Assess for parasitized red blood cells.
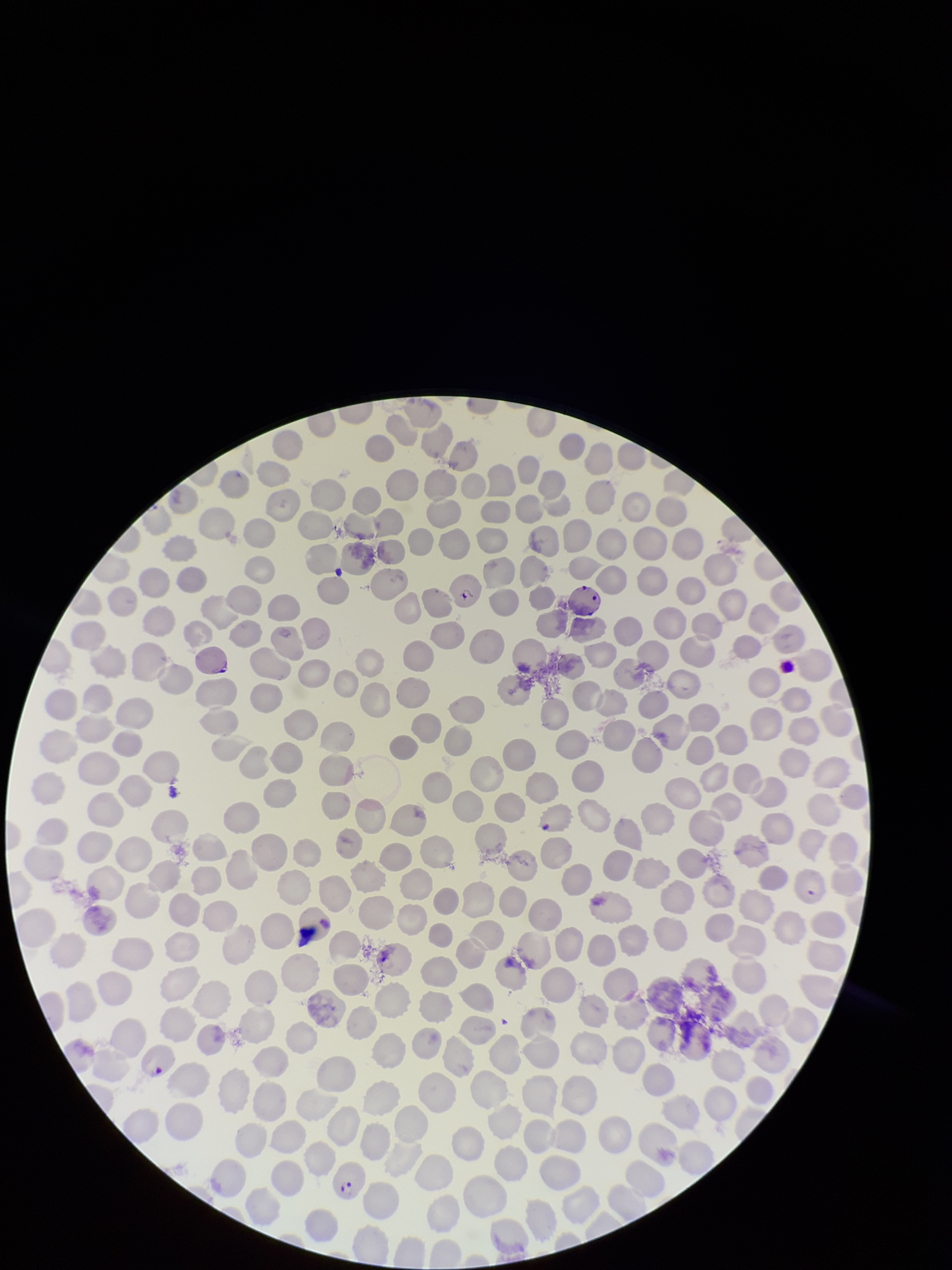

Identified.

red blood cell count = 252
field of view = one from this slide
species reported for this patient = Plasmodium falciparum
parasitized red blood cell count = 4
patient malaria status = positive
preparation = thin blood smear
image size = 952×1270 pixels
capture = smartphone photograph through the microscope eyepiece
stain = Giemsa